Report the malaria status of this cell.
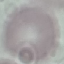
Uninfected.

stain = Giemsa
capture = smartphone through the microscope eyepiece
preparation = thin blood film
image type = automatically extracted cell patch, resized to 64 × 64 pixels